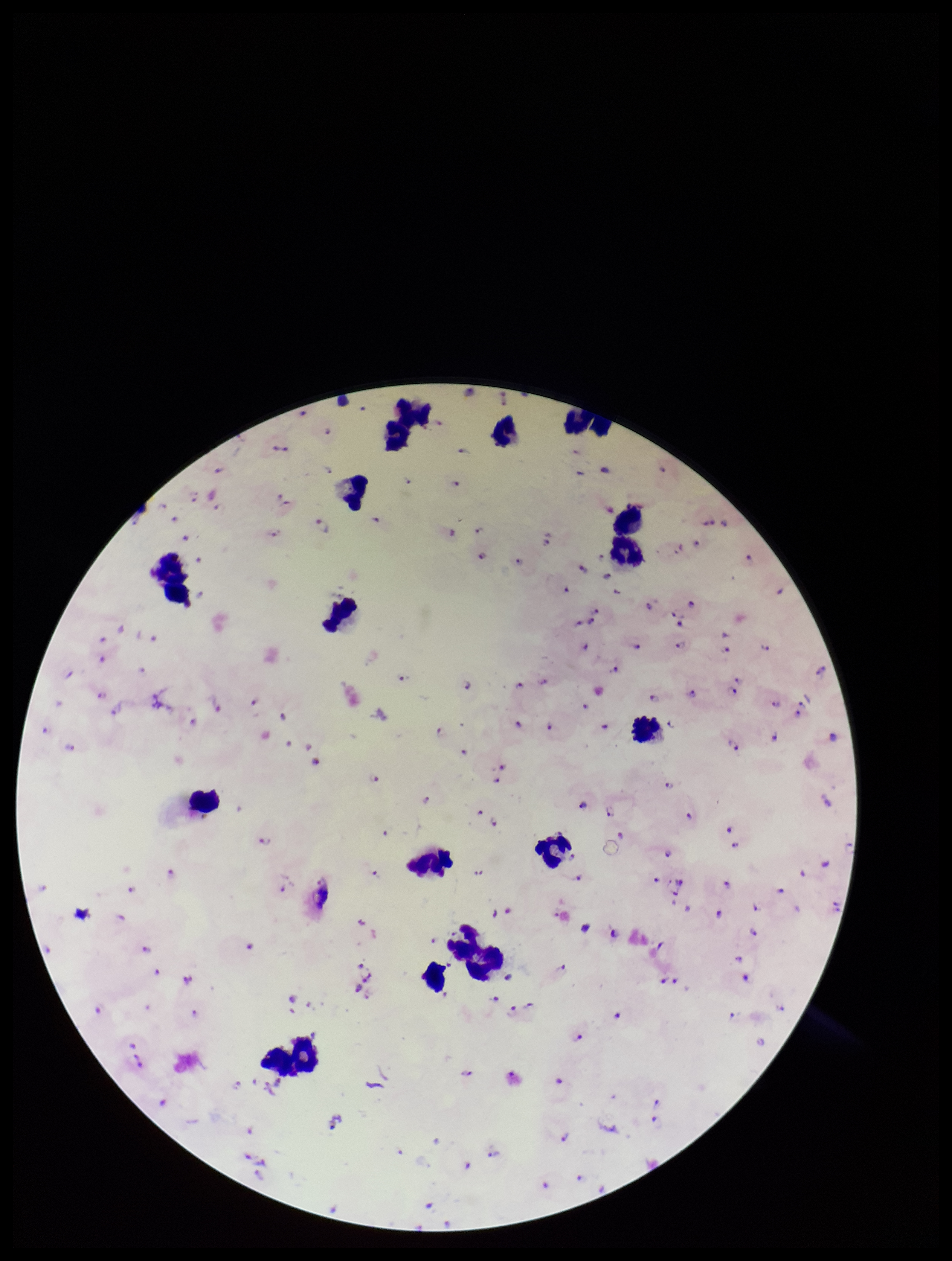

Smartphone photograph taken through the eyepiece of a microscope. Leukocyte count: 17. Species reported for this patient: Plasmodium falciparum. Stained with Giemsa. Preparation: thick blood smear. Image is 952×1261 pixels. Parasite count: 96. Patient malaria status: infected. Single field of view. Plasmodium parasites: detected.